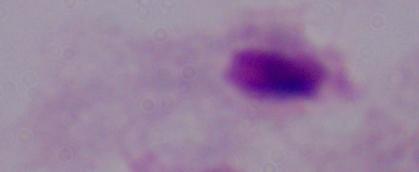
magnification: 1000x
modality: micrograph
identification: trichomonad